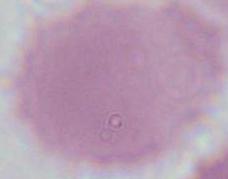

Summary:
  - Magnification: 1000x
  - Modality: photomicrograph
  - Identification: erythrocyte